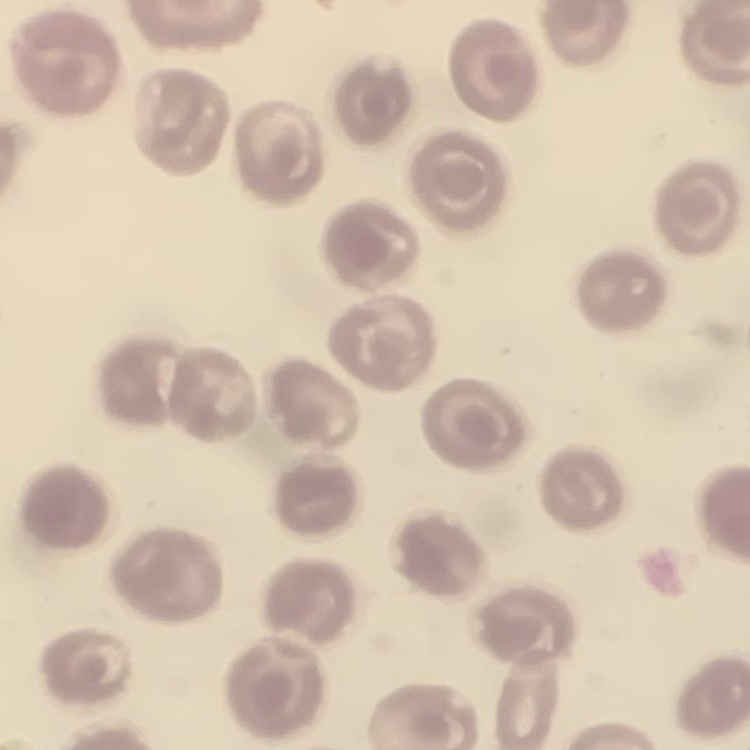

{
  "erythrocyte_morphology": "no rouleaux formation",
  "preparation": "thin blood film",
  "image_type": "square crop of a larger photomicrograph",
  "stain": "Field's or Giemsa"
}